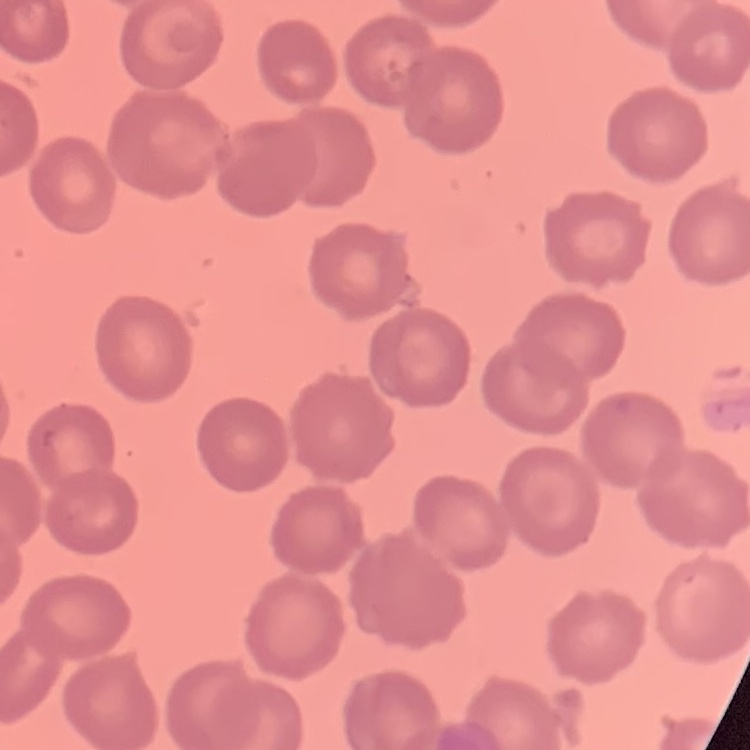

Summary:
  - Red blood cell morphology: no rouleaux formation
  - Preparation: thin peripheral smear
  - Image type: one tile cut from a larger photomicrograph
  - Stain: Field's or Giemsa